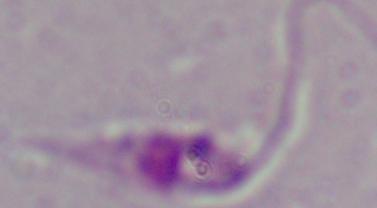
1000x magnification. A Leishmania parasite is shown. Photomicrograph.